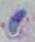
Summary:
  - Magnification: 1000x
  - Modality: photomicrograph
  - Identification: Toxoplasma gondii